Name the blood parasite species.
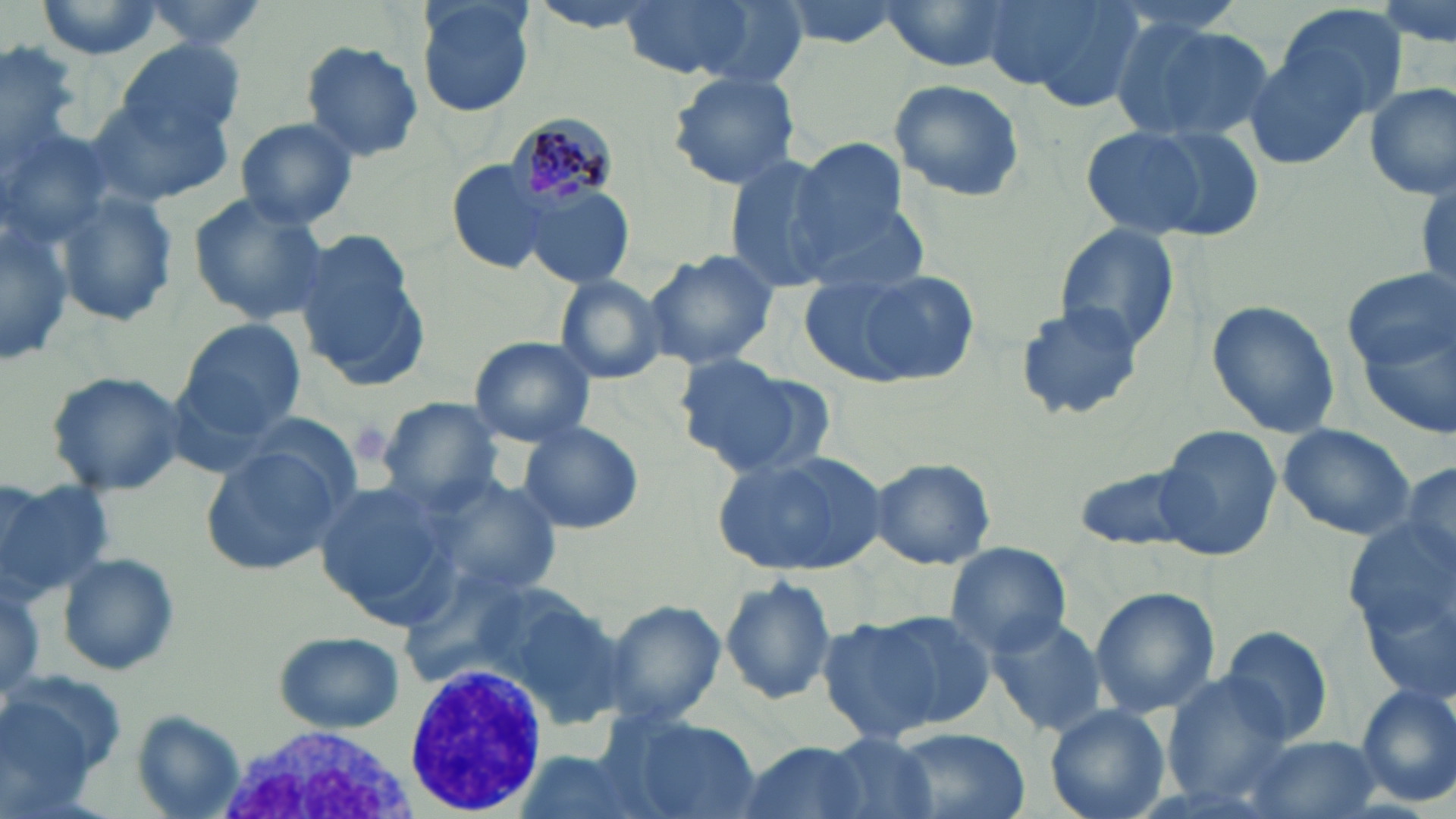
Plasmodium malariae.

Approximate bounding boxes as (x1, y1, x2, y2) in pixels. White blood cell locations: (402, 660, 550, 814), (222, 724, 413, 819). Plasmodium malariae-infected red blood cell locations: (505, 112, 617, 211). Uninfected red blood cell locations: (31, 0, 168, 60), (137, 0, 270, 55), (415, 0, 535, 117), (524, 0, 668, 34), (619, 0, 761, 80), (771, 0, 913, 47), (878, 0, 1020, 72), (981, 0, 1145, 108), (1378, 0, 1453, 58), (1273, 2, 1409, 122), (1108, 13, 1273, 143), (1, 39, 82, 176), (115, 39, 245, 145), (298, 40, 424, 162), (1244, 47, 1370, 170), (665, 68, 802, 190), (889, 79, 1026, 204), (1363, 82, 1455, 201), (90, 92, 235, 205), (233, 117, 359, 230), (0, 118, 116, 258), (1078, 124, 1244, 242), (791, 149, 922, 286), (720, 154, 847, 287), (444, 160, 553, 274), (522, 185, 636, 289), (53, 192, 179, 327), (187, 192, 331, 323), (0, 207, 76, 369), (1053, 223, 1178, 354), (295, 235, 431, 391), (643, 253, 779, 370), (1342, 267, 1452, 378), (818, 268, 979, 387), (550, 274, 667, 384), (1204, 300, 1341, 437), (1012, 302, 1147, 422), (1360, 312, 1456, 449), (180, 319, 306, 436), (468, 336, 596, 446), (674, 356, 829, 476), (45, 369, 187, 497), (376, 397, 505, 508), (224, 414, 369, 511), (516, 419, 645, 533), (1276, 424, 1417, 543), (1156, 425, 1281, 562), (199, 445, 347, 578), (716, 448, 888, 576), (868, 458, 996, 569), (1399, 459, 1455, 573), (1069, 460, 1209, 554), (421, 474, 565, 605), (1, 475, 116, 602), (313, 481, 453, 620), (945, 543, 1072, 657), (56, 552, 181, 676), (718, 573, 838, 706), (0, 576, 45, 710), (1089, 587, 1218, 718), (604, 600, 726, 725), (826, 610, 986, 739), (984, 615, 1106, 737), (1218, 625, 1335, 747), (273, 631, 405, 734), (5, 670, 130, 797), (1159, 676, 1295, 804), (1354, 683, 1456, 809), (1045, 705, 1170, 819), (132, 710, 248, 819), (600, 712, 760, 819), (888, 728, 1028, 819), (1239, 734, 1381, 819), (780, 735, 939, 819), (733, 739, 875, 819), (507, 745, 663, 819). Thin blood smear. Image is 1456×819 pixels. Single field of view. May-Grünwald-Giemsa stain. 1000x magnification. Light microscopy.